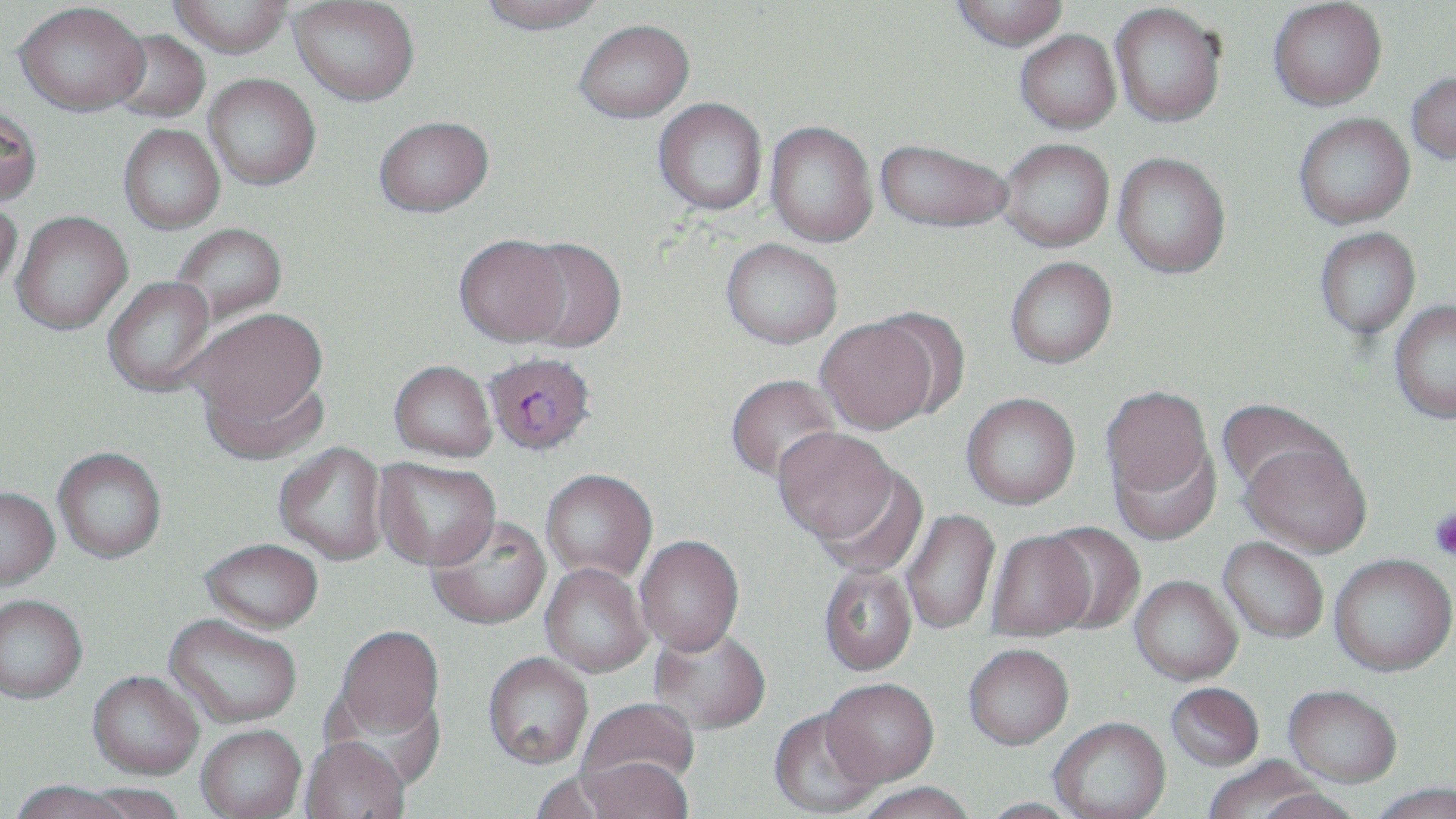
slide-level diagnosis = Plasmodium falciparum
image size = 1456×819 pixels
Plasmodium falciparum-infected red blood cell locations = approximate bounding boxes as (x1,y1)-(x2,y2) corner pairs in pixels: (483,352)-(597,459)
modality = light microscopy
preparation = thin blood smear
magnification = 1000x
uninfected red blood cell locations = approximate bounding boxes as (x1,y1)-(x2,y2) corner pairs in pixels: (169,0)-(293,58), (477,0)-(607,34), (952,0)-(1069,51), (1268,0)-(1387,111), (290,1)-(420,105), (15,2)-(149,116), (1110,3)-(1227,127), (575,19)-(694,123), (107,28)-(210,123), (1015,29)-(1120,134), (1406,71)-(1456,164), (204,74)-(321,190), (653,98)-(767,215), (0,103)-(43,207), (1293,113)-(1415,229), (373,116)-(493,217), (765,121)-(877,247), (118,124)-(224,234), (875,138)-(1014,233), (997,139)-(1114,252), (1113,152)-(1231,278), (0,193)-(23,296), (11,212)-(132,335), (169,223)-(287,327), (1315,226)-(1420,339), (454,234)-(571,346), (516,237)-(627,352), (721,238)-(843,348), (1005,256)-(1117,368), (102,277)-(217,396), (1389,299)-(1456,424), (184,307)-(328,432), (816,316)-(939,435), (389,361)-(497,464), (199,369)-(330,465), (725,373)-(842,484), (1101,386)-(1214,501), (961,393)-(1081,510), (1216,398)-(1345,500), (774,428)-(899,549), (1109,437)-(1222,546), (1241,439)-(1373,557), (274,444)-(388,566), (53,449)-(166,566), (374,459)-(501,574), (813,466)-(930,580), (540,471)-(657,585), (0,488)-(59,591), (901,509)-(1000,635), (425,517)-(552,633), (1040,521)-(1146,634), (986,531)-(1096,641), (1218,536)-(1329,643), (635,538)-(745,660), (198,542)-(323,636), (1330,553)-(1456,676), (540,565)-(652,679), (818,566)-(917,677), (1130,575)-(1243,685), (0,598)-(87,706), (163,616)-(301,730), (335,628)-(444,742), (649,628)-(770,737), (963,645)-(1073,752), (482,655)-(593,772), (87,674)-(202,782), (821,682)-(939,790), (1165,682)-(1265,771), (1283,684)-(1403,787), (576,702)-(699,810), (768,710)-(882,817), (1050,719)-(1172,819), (196,728)-(306,818), (299,740)-(409,819), (1200,755)-(1331,818), (573,762)-(694,818), (529,771)-(629,819), (8,784)-(134,819), (77,784)-(186,819), (853,786)-(979,819), (975,800)-(1086,819)
field of view = single
platelet locations = approximate bounding boxes as (x1,y1)-(x2,y2) corner pairs in pixels: (1429,506)-(1456,562)
stain = May-Grünwald-Giemsa